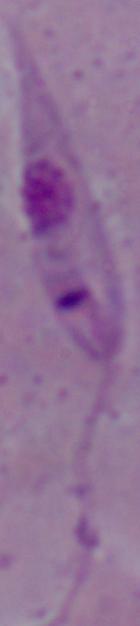

Summary:
  - Modality: photomicrograph
  - Magnification: 1000x
  - Identification: Leishmania